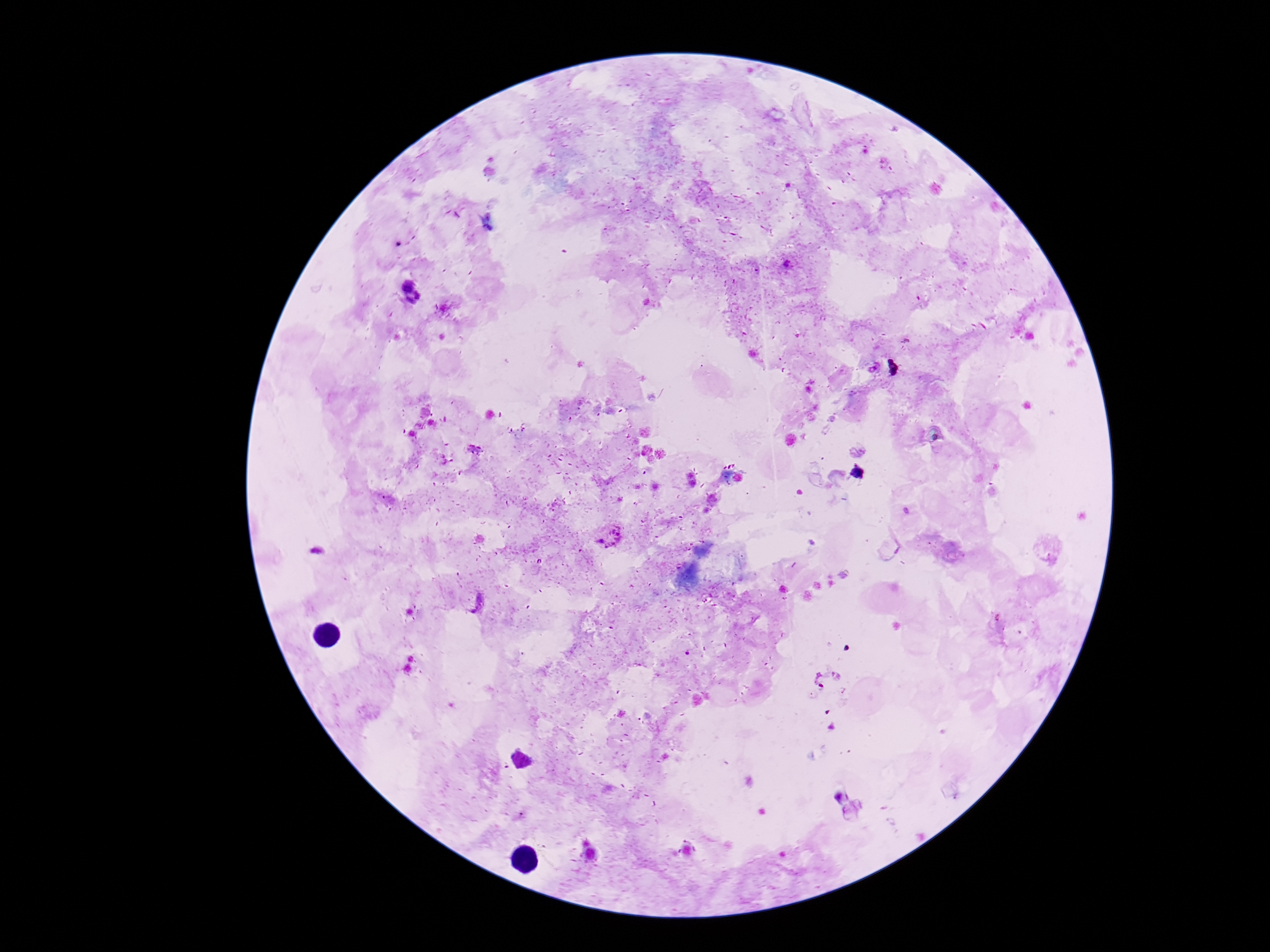
Approximate centers as [x, y] in pixels. Plasmodium parasite locations: [788, 264], [608, 536], [475, 602], [827, 679]. Single field of view. Thick peripheral-blood smear. Giemsa-stained preparation. Photographed through the microscope eyepiece with a smartphone camera. 100x magnification. Patient malaria status: positive. Image is 1270×952 pixels.